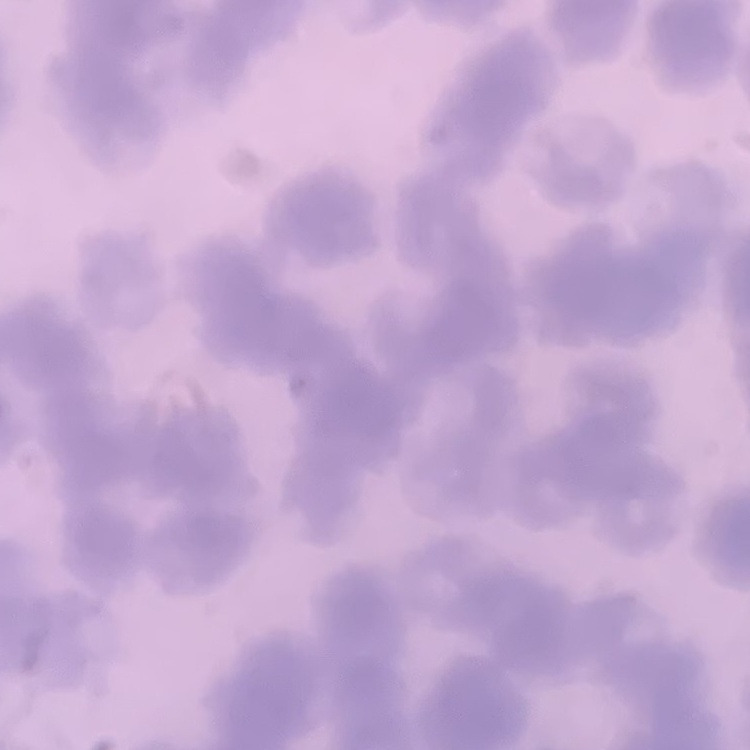

red blood cell morphology = rouleaux formation
stain = Field's or Giemsa
preparation = thin blood smear
image type = square crop of a larger photomicrograph